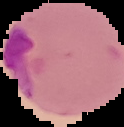

Image is 124×127 pixels. The area outside the segmented cell region is set to black. From a thin blood film. Malaria status: parasitized.